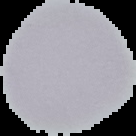

preparation: thin blood smear
image_size: 136×136 pixels
image_type: segmented cell region with the area outside set to black
result: negative for Plasmodium parasites